Give the extent of all Plasmodium falciparum-infected red blood cells.
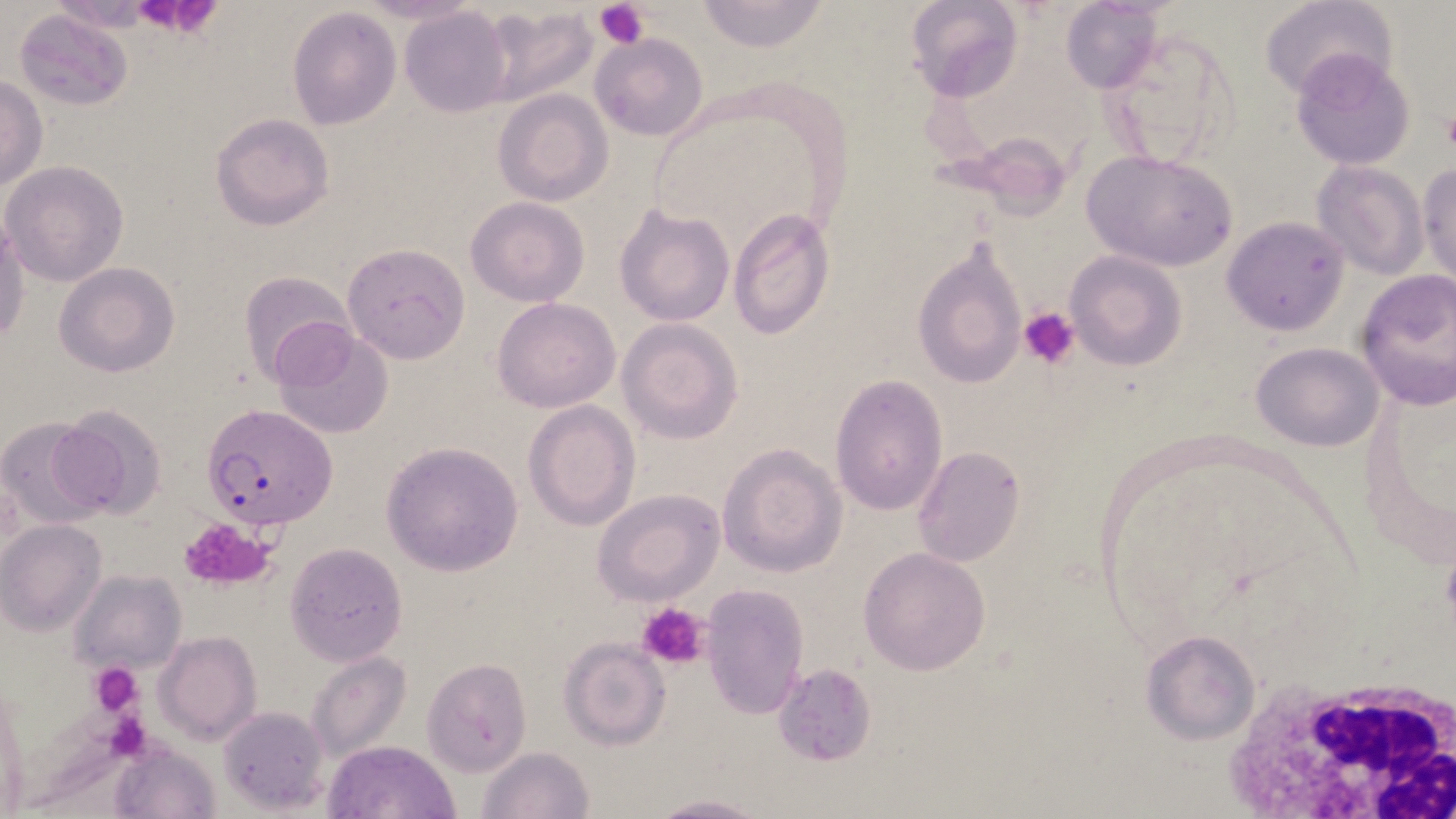

Approximate bounding boxes as named x1/y1/x2/y2 corners in pixels.
Plasmodium falciparum-infected red blood cells: (x1=203, y1=405, x2=337, y2=529).

Summary:
  - Platelet locations: (x1=126, y1=0, x2=225, y2=37), (x1=595, y1=0, x2=649, y2=47), (x1=1440, y1=112, x2=1456, y2=155), (x1=1018, y1=308, x2=1079, y2=368), (x1=176, y1=517, x2=278, y2=592), (x1=636, y1=600, x2=709, y2=670), (x1=90, y1=663, x2=140, y2=716)
  - Uninfected red blood cell locations: (x1=903, y1=0, x2=1022, y2=104), (x1=693, y1=1, x2=831, y2=53), (x1=1060, y1=1, x2=1163, y2=95), (x1=1262, y1=1, x2=1395, y2=100), (x1=287, y1=6, x2=403, y2=130), (x1=399, y1=6, x2=514, y2=117), (x1=478, y1=6, x2=598, y2=106), (x1=12, y1=8, x2=134, y2=111), (x1=1100, y1=25, x2=1241, y2=167), (x1=591, y1=33, x2=708, y2=141), (x1=1291, y1=49, x2=1415, y2=171), (x1=0, y1=76, x2=47, y2=192), (x1=493, y1=89, x2=613, y2=205), (x1=211, y1=113, x2=334, y2=232), (x1=1080, y1=150, x2=1239, y2=272), (x1=1311, y1=159, x2=1430, y2=279), (x1=1417, y1=161, x2=1455, y2=286), (x1=3, y1=162, x2=128, y2=286), (x1=465, y1=196, x2=590, y2=307), (x1=615, y1=203, x2=734, y2=327), (x1=726, y1=207, x2=835, y2=340), (x1=0, y1=215, x2=29, y2=349), (x1=1223, y1=216, x2=1350, y2=336), (x1=913, y1=240, x2=1029, y2=391), (x1=342, y1=243, x2=471, y2=364), (x1=1064, y1=252, x2=1187, y2=370), (x1=54, y1=262, x2=180, y2=378), (x1=1354, y1=268, x2=1456, y2=410), (x1=240, y1=270, x2=355, y2=384), (x1=492, y1=297, x2=620, y2=413), (x1=617, y1=319, x2=743, y2=444), (x1=271, y1=327, x2=395, y2=442), (x1=1250, y1=342, x2=1385, y2=451), (x1=830, y1=375, x2=947, y2=515), (x1=522, y1=399, x2=641, y2=531), (x1=50, y1=403, x2=169, y2=523), (x1=2, y1=417, x2=107, y2=527), (x1=382, y1=442, x2=523, y2=577), (x1=717, y1=442, x2=847, y2=577), (x1=913, y1=446, x2=1025, y2=566), (x1=593, y1=489, x2=726, y2=607), (x1=2, y1=519, x2=107, y2=635), (x1=285, y1=542, x2=408, y2=666), (x1=859, y1=546, x2=991, y2=675), (x1=72, y1=569, x2=187, y2=677), (x1=699, y1=582, x2=809, y2=719), (x1=1140, y1=629, x2=1259, y2=744), (x1=154, y1=631, x2=261, y2=745), (x1=559, y1=637, x2=671, y2=751), (x1=306, y1=651, x2=411, y2=761), (x1=423, y1=658, x2=532, y2=775), (x1=773, y1=663, x2=878, y2=766), (x1=218, y1=706, x2=327, y2=810), (x1=112, y1=739, x2=220, y2=819), (x1=323, y1=739, x2=460, y2=819), (x1=478, y1=746, x2=594, y2=819), (x1=640, y1=793, x2=768, y2=819)
  - White blood cell locations: (x1=1217, y1=671, x2=1456, y2=819)
  - Slide-level diagnosis: Plasmodium falciparum
  - Modality: optical microscopy
  - Magnification: 1000x
  - Field of view: single
  - Preparation: thin blood smear
  - Stain: May-Grünwald-Giemsa
  - Image size: 1456×819 pixels